Report the malaria status of this cell.
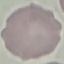
It is uninfected.

Giemsa stain. Thin blood smear. Acquired by smartphone through the microscope eyepiece. Automatically extracted cell patch, resized to 64 × 64 pixels.